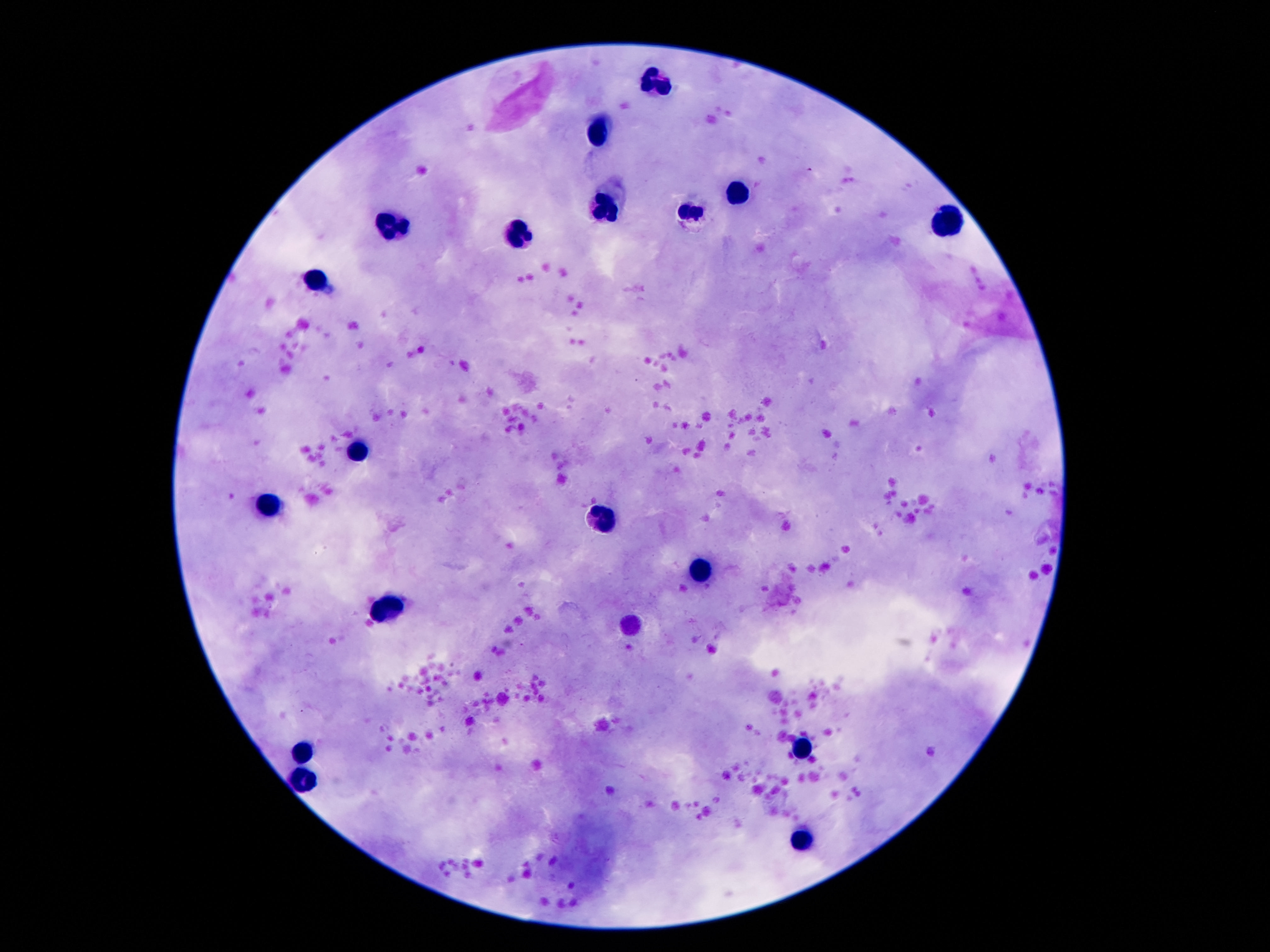
Approximate centers as [x, y] in pixels.
Summary:
  - Leukocyte locations: [656, 76], [597, 133], [740, 194], [603, 211], [687, 211], [950, 219], [393, 223], [521, 235], [317, 278], [361, 446], [271, 504], [601, 521], [702, 573], [389, 608], [632, 628], [307, 746], [805, 752], [303, 778], [803, 841]
  - Stain: Giemsa
  - Field of view: single
  - Image size: 1270×952 pixels
  - Capture: smartphone camera through the microscope eyepiece
  - Patient malaria status: not infected
  - Preparation: thick blood film
  - Magnification: 100x